Outline platelets.
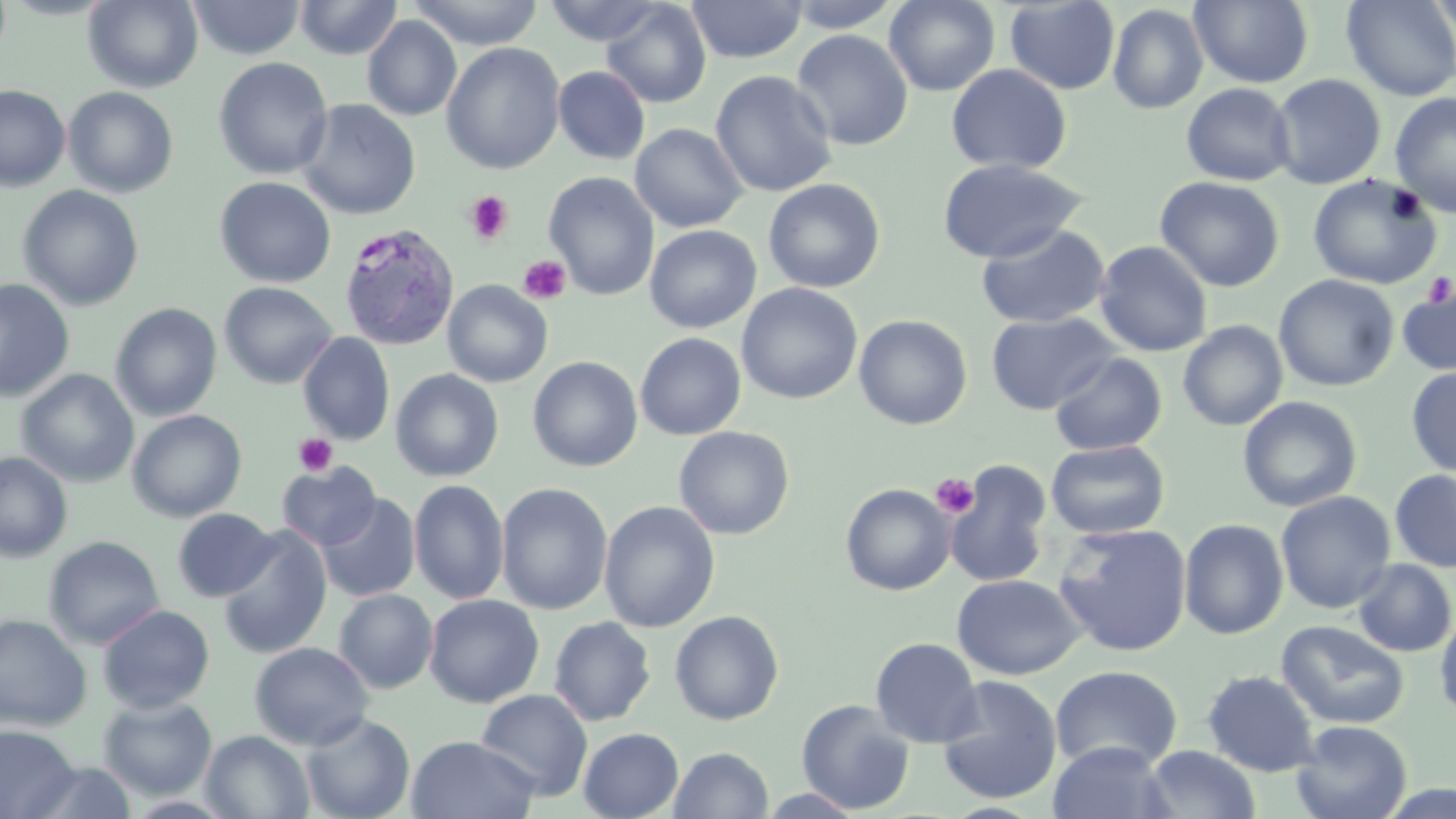
Approximate bounding boxes as (x1,y1)-(x2,y2) corner pairs in pixels.
Platelets: (463,191)-(513,245), (518,255)-(572,305), (1422,273)-(1456,305), (293,433)-(337,477), (931,473)-(979,518).

slide-level diagnosis = Plasmodium vivax
preparation = thin blood smear
uninfected red blood cell locations = approximate bounding boxes as (x1,y1)-(x2,y2) corner pairs in pixels: (83,0)-(203,93), (294,0)-(403,60), (408,0)-(546,50), (543,0)-(668,47), (686,0)-(806,63), (783,0)-(904,33), (884,0)-(1000,96), (1189,0)-(1314,88), (1341,0)-(1456,102), (186,1)-(306,60), (601,1)-(712,108), (1004,1)-(1120,94), (1425,1)-(1456,45), (1108,4)-(1208,114), (362,16)-(462,120), (791,29)-(914,151), (441,43)-(566,174), (213,57)-(333,179), (946,64)-(1072,175), (553,66)-(650,164), (711,70)-(838,197), (1268,74)-(1386,190), (1181,82)-(1296,186), (0,84)-(71,191), (63,86)-(178,198), (1389,92)-(1456,217), (296,98)-(421,220), (630,123)-(747,233), (936,158)-(1087,263), (544,172)-(659,300), (1308,174)-(1441,290), (214,176)-(336,288), (1155,176)-(1284,292), (763,178)-(885,293), (18,184)-(144,311), (976,224)-(1111,328), (644,225)-(761,333), (1094,240)-(1212,357), (1273,274)-(1399,392), (1397,277)-(1456,378), (0,278)-(75,402), (442,279)-(553,387), (219,282)-(337,388), (736,283)-(863,404), (110,302)-(222,422), (985,312)-(1118,415), (854,314)-(972,430), (1177,321)-(1288,431), (298,332)-(395,445), (635,332)-(746,440), (1049,352)-(1167,456), (528,356)-(643,472), (1406,366)-(1456,477), (390,368)-(504,482), (16,369)-(139,487), (1237,395)-(1362,513), (127,409)-(247,522), (673,426)-(794,540), (1046,440)-(1169,539), (0,451)-(73,563), (944,460)-(1053,588), (277,461)-(381,550), (1390,469)-(1456,572), (409,479)-(509,605), (496,482)-(613,616), (841,483)-(956,596), (1275,491)-(1396,614), (316,493)-(421,602), (599,500)-(720,633), (172,508)-(279,602), (1178,519)-(1289,640), (1053,522)-(1193,657), (216,525)-(333,659), (43,535)-(165,649), (1353,558)-(1455,657), (951,574)-(1086,680), (333,589)-(438,694), (424,595)-(544,708), (97,604)-(215,714), (1435,607)-(1456,723), (669,610)-(784,725), (0,614)-(93,731), (548,616)-(656,726), (1275,620)-(1411,730), (870,637)-(983,748), (249,642)-(374,750), (1049,665)-(1183,773), (1202,670)-(1319,777), (936,675)-(1063,804), (475,689)-(593,801), (98,696)-(218,800), (796,699)-(915,814), (300,713)-(415,819), (1290,720)-(1413,819), (0,724)-(79,819), (578,727)-(684,819), (201,730)-(315,818), (405,734)-(540,819), (1047,740)-(1175,819), (1141,745)-(1261,818), (668,747)-(773,819), (24,761)-(137,818), (1377,780)-(1456,818), (758,788)-(868,817)
modality = optical microscopy
stain = May-Grünwald-Giemsa
magnification = 1000x
image size = 1456×819 pixels
field of view = single
Plasmodium vivax-infected red blood cell locations = approximate bounding boxes as (x1,y1)-(x2,y2) corner pairs in pixels: (338,222)-(460,351)